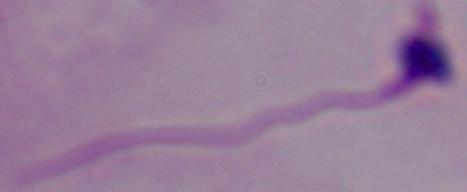
Summary:
  - Identification: Leishmania
  - Modality: micrograph
  - Magnification: 1000x